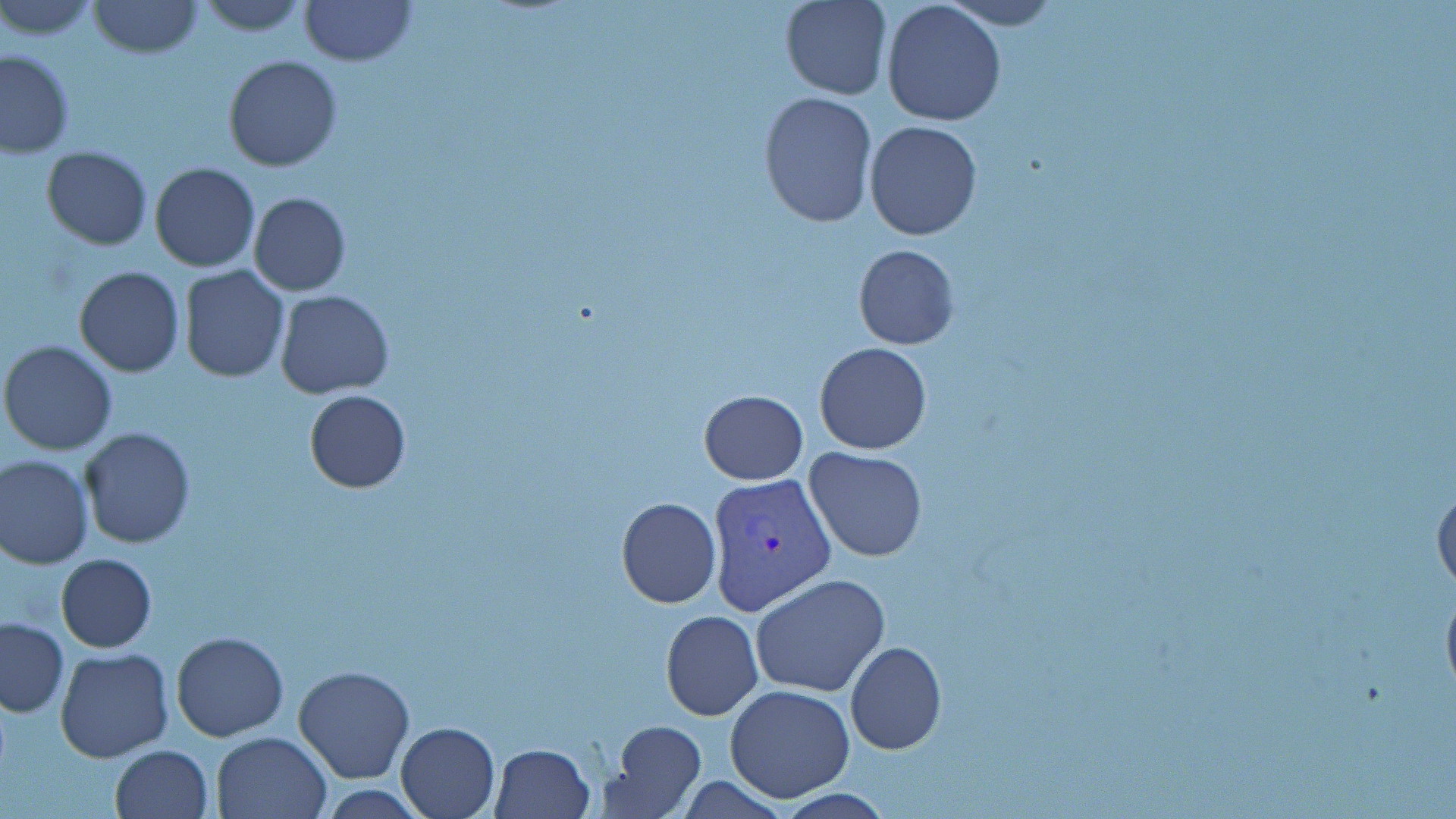

Approximate bounding boxes as (x1, y1, x2, y2) in pixels. Plasmodium vivax-infected red blood cell locations: (706, 471, 835, 616). Uninfected red blood cell locations: (1, 0, 102, 41), (193, 0, 312, 36), (298, 0, 416, 67), (780, 0, 891, 100), (939, 0, 1064, 30), (87, 1, 202, 58), (879, 1, 1007, 128), (0, 48, 74, 157), (223, 54, 342, 172), (757, 90, 878, 227), (865, 120, 982, 240), (41, 145, 152, 250), (149, 162, 260, 272), (247, 192, 349, 296), (853, 244, 959, 349), (74, 265, 184, 377), (179, 266, 289, 382), (274, 288, 395, 398), (25, 298, 141, 432), (1, 341, 118, 456), (813, 342, 932, 455), (699, 389, 807, 485), (304, 391, 412, 493), (78, 427, 196, 549), (803, 447, 929, 563), (0, 454, 94, 569), (1433, 479, 1456, 598), (616, 497, 721, 608), (55, 553, 157, 652), (751, 571, 891, 698), (661, 610, 762, 720), (0, 618, 69, 718), (171, 632, 289, 741), (845, 641, 947, 755), (55, 649, 174, 763), (293, 664, 416, 784), (723, 685, 856, 801), (395, 720, 501, 819), (607, 721, 706, 815), (211, 730, 332, 818), (490, 743, 596, 818), (109, 744, 214, 819), (316, 784, 431, 817). Slide-level diagnosis: Plasmodium vivax. May-Grünwald-Giemsa stain. Captured at 1000x magnification. Thin blood film. Image is 1456×819 pixels. Light microscopy. Single field of view.